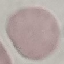 Malaria status: uninfected. Thin blood film. Photographed with a smartphone camera at the microscope eyepiece. Giemsa stain. Cell patch, automatically extracted from a larger field of view and resized to 64 × 64 pixels.